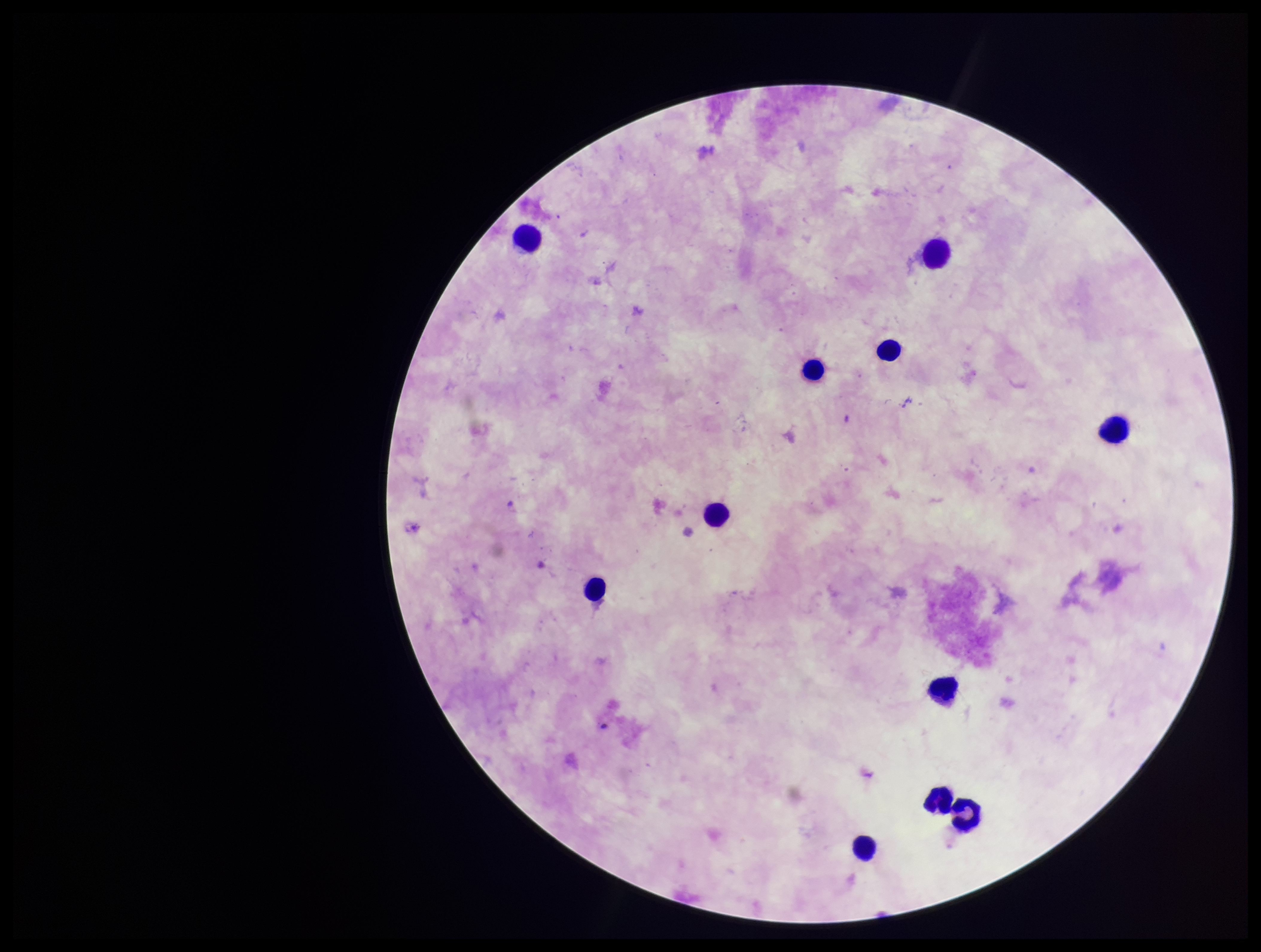

image_size: 1261×952 pixels
plasmodium_parasites: none seen
stain: Giemsa
field_of_view: one from this slide
preparation: thick blood smear
parasite_count: 0
patient_malaria_status: negative
leukocyte_count: 11
capture: smartphone photograph through the microscope eyepiece